Name the cell type shown.
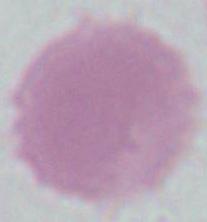

This is an erythrocyte.

Micrograph. 1000x magnification.